Assess this cell for malaria.
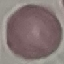
It is uninfected.

Summary:
  - Stain: Giemsa
  - Preparation: thin blood film
  - Image type: automatically extracted cell patch, resized to 64 × 64 pixels
  - Capture: smartphone through the microscope eyepiece